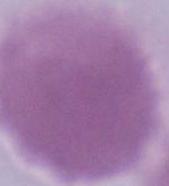

magnification: 1000x
identification: red blood cell
modality: photomicrograph